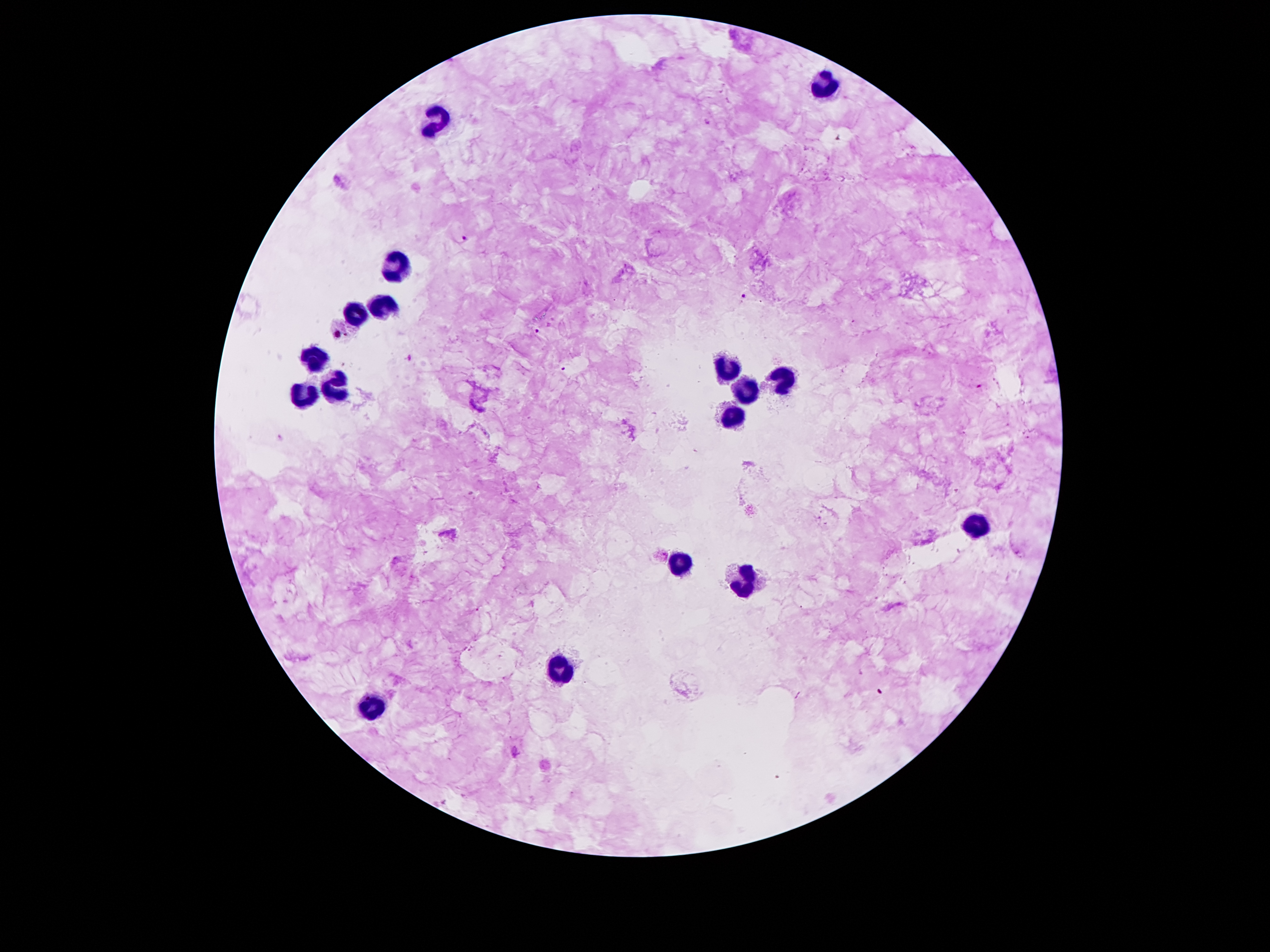 Approximate centers as {x, y} in pixels. Leukocyte locations: {823, 80}, {437, 119}, {389, 265}, {381, 306}, {353, 314}, {314, 360}, {725, 366}, {781, 379}, {333, 382}, {742, 391}, {300, 396}, {728, 424}, {980, 522}, {675, 564}, {739, 586}, {557, 674}, {367, 704}. Malaria parasite locations: {707, 122}, {466, 240}, {746, 296}, {535, 332}, {339, 337}, {563, 368}, {978, 385}. Photographed through the microscope eyepiece with a smartphone camera. Patient malaria status: positive for Plasmodium falciparum. Thick blood smear. Image is 1270×952 pixels. 100x magnification. Giemsa stain. Single field of view.